Classify this cell by malaria status.
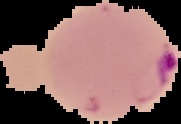
Parasitized.

Summary:
  - Image size: 181×124 pixels
  - Image type: segmented cell region with the area outside set to black
  - Preparation: thin blood smear